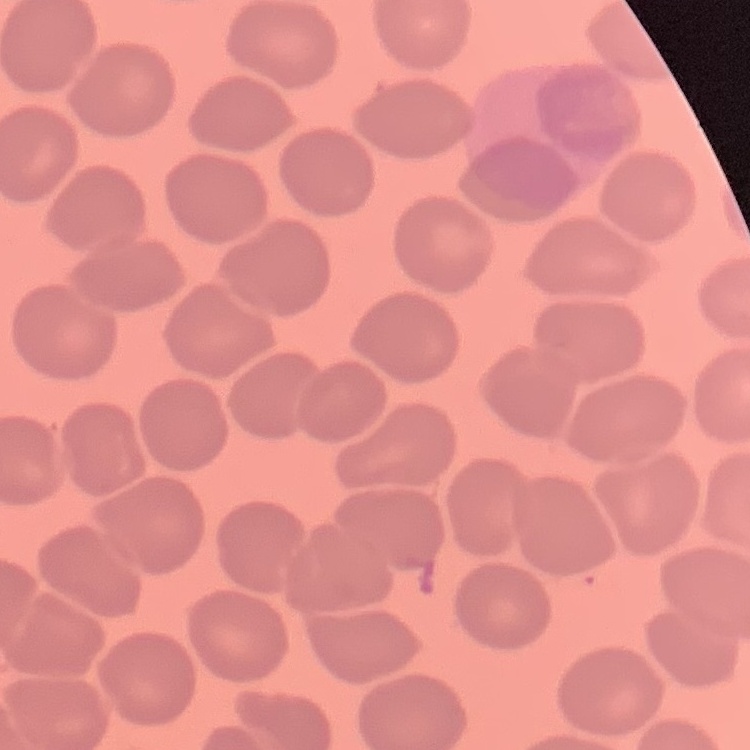

{
  "red_blood_cell_morphology": "no rouleaux formation",
  "image_type": "square crop of a larger photomicrograph",
  "stain": "Field's or Giemsa",
  "preparation": "thin blood smear"
}